Report the malaria status of this cell.
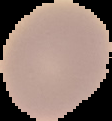
It is uninfected.

image type = segmented cell region on a black background
image size = 112×121 pixels
preparation = thin blood film